Locate every blood parasite and identify its species.
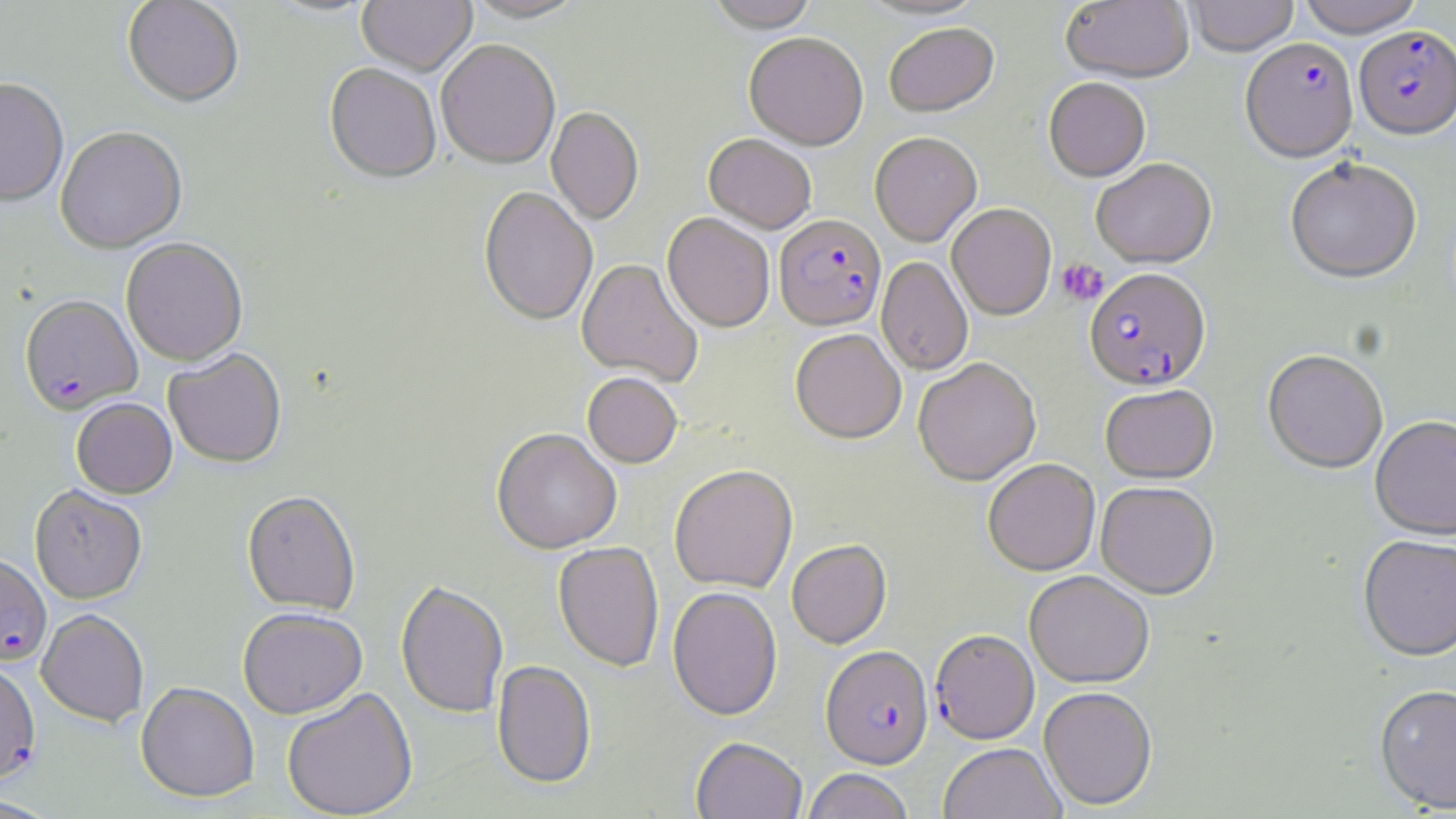

Approximate bounding boxes as named x1/y1/x2/y2 corners in pixels.
Plasmodium falciparum-infected red blood cells: (x1=1354, y1=27, x2=1456, y2=142), (x1=1240, y1=38, x2=1359, y2=165), (x1=774, y1=214, x2=886, y2=330), (x1=1085, y1=268, x2=1211, y2=392), (x1=20, y1=296, x2=142, y2=415), (x1=0, y1=553, x2=52, y2=666), (x1=930, y1=629, x2=1039, y2=745), (x1=821, y1=646, x2=933, y2=769), (x1=0, y1=658, x2=41, y2=787).
No Plasmodium ovale, Plasmodium malariae, Plasmodium vivax, Babesia divergens, or Trypanosoma brucei observed.

Uninfected red blood cell locations: (x1=122, y1=0, x2=244, y2=109), (x1=264, y1=0, x2=378, y2=19), (x1=357, y1=0, x2=476, y2=77), (x1=462, y1=0, x2=591, y2=23), (x1=705, y1=0, x2=820, y2=31), (x1=1060, y1=0, x2=1194, y2=84), (x1=1185, y1=0, x2=1299, y2=57), (x1=1296, y1=0, x2=1425, y2=38), (x1=884, y1=23, x2=999, y2=116), (x1=744, y1=32, x2=868, y2=149), (x1=436, y1=41, x2=560, y2=169), (x1=324, y1=64, x2=441, y2=185), (x1=1043, y1=77, x2=1151, y2=182), (x1=0, y1=79, x2=69, y2=208), (x1=546, y1=107, x2=643, y2=224), (x1=55, y1=129, x2=187, y2=254), (x1=870, y1=132, x2=982, y2=247), (x1=704, y1=133, x2=816, y2=233), (x1=1091, y1=159, x2=1217, y2=269), (x1=1285, y1=160, x2=1422, y2=286), (x1=479, y1=187, x2=598, y2=326), (x1=947, y1=203, x2=1056, y2=320), (x1=662, y1=213, x2=775, y2=332), (x1=121, y1=239, x2=247, y2=366), (x1=877, y1=257, x2=973, y2=376), (x1=577, y1=258, x2=703, y2=387), (x1=790, y1=328, x2=906, y2=444), (x1=163, y1=349, x2=287, y2=468), (x1=1262, y1=351, x2=1388, y2=475), (x1=913, y1=358, x2=1041, y2=486), (x1=582, y1=372, x2=683, y2=468), (x1=1100, y1=384, x2=1218, y2=484), (x1=72, y1=398, x2=177, y2=499), (x1=1370, y1=417, x2=1456, y2=541), (x1=491, y1=428, x2=622, y2=554), (x1=983, y1=459, x2=1100, y2=576), (x1=669, y1=464, x2=798, y2=593), (x1=1095, y1=482, x2=1219, y2=599), (x1=30, y1=486, x2=147, y2=604), (x1=242, y1=491, x2=361, y2=616), (x1=1358, y1=537, x2=1456, y2=665), (x1=786, y1=540, x2=892, y2=649), (x1=553, y1=542, x2=665, y2=672), (x1=1024, y1=571, x2=1154, y2=689), (x1=396, y1=580, x2=509, y2=719), (x1=667, y1=587, x2=782, y2=721), (x1=238, y1=607, x2=368, y2=719), (x1=36, y1=609, x2=149, y2=727), (x1=492, y1=660, x2=597, y2=788), (x1=136, y1=682, x2=259, y2=803), (x1=1374, y1=686, x2=1456, y2=815), (x1=281, y1=687, x2=418, y2=819), (x1=1038, y1=687, x2=1157, y2=811), (x1=690, y1=737, x2=808, y2=819), (x1=939, y1=743, x2=1065, y2=819), (x1=801, y1=769, x2=914, y2=819), (x1=0, y1=795, x2=60, y2=817). Platelet locations: (x1=1057, y1=258, x2=1108, y2=306). Slide-level diagnosis: Plasmodium falciparum. Captured at 1000x magnification. Single field of view. Thin blood smear. Optical microscopy. May-Grünwald-Giemsa stain. Image is 1456×819 pixels.